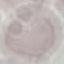

Result: no malaria parasites seen. Thin blood smear. Acquired by smartphone through the microscope eyepiece. Automatically extracted cell patch, resized to 64 × 64 pixels. Giemsa-stained preparation.